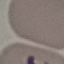
Summary:
  - Malaria status: parasitized
  - Stain: Giemsa
  - Image type: automatically extracted cell patch, resized to 64 × 64 pixels
  - Capture: smartphone through the microscope eyepiece
  - Preparation: thin smear